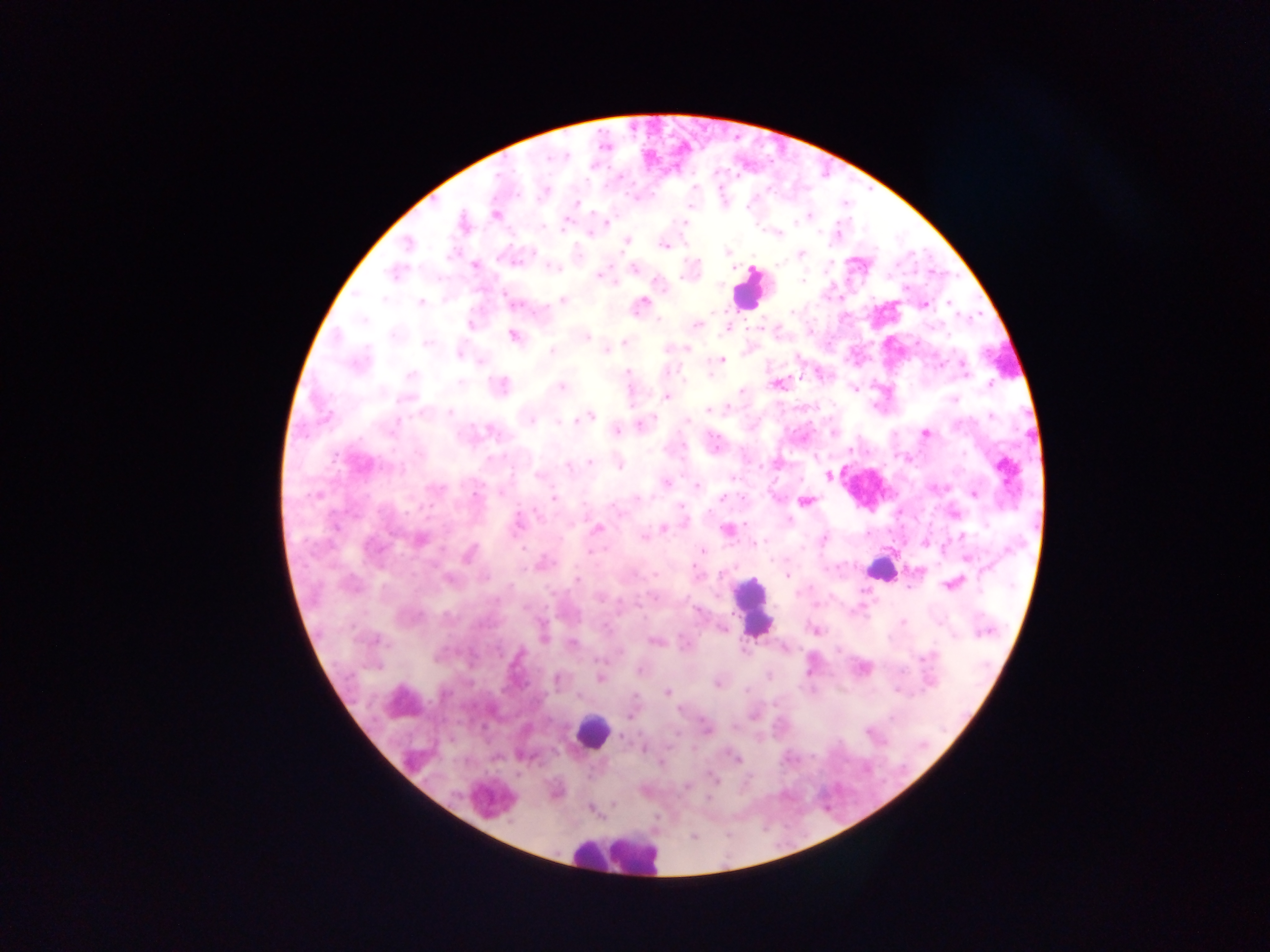

Approximate centers as {x, y} in pixels.
Summary:
  - Plasmodium parasite locations: {606, 147}, {622, 178}, {575, 202}, {496, 213}, {807, 216}, {805, 219}, {682, 223}, {544, 226}, {563, 227}, {590, 233}, {777, 235}, {626, 242}, {664, 245}, {726, 252}, {801, 254}, {852, 258}, {858, 259}, {518, 260}, {475, 265}, {631, 267}, {395, 273}, {597, 275}, {805, 279}, {356, 291}, {384, 297}, {561, 299}, {507, 301}, {641, 303}, {421, 304}, {925, 305}, {793, 313}, {363, 319}, {697, 322}, {726, 330}, {512, 335}, {585, 337}, {623, 340}, {426, 343}, {666, 348}, {605, 350}, {552, 352}, {459, 354}, {721, 358}, {479, 363}, {668, 370}, {625, 371}, {409, 375}, {777, 383}, {988, 383}, {499, 385}, {561, 387}, {740, 391}, {668, 397}, {405, 398}, {953, 400}, {715, 409}, {708, 410}, {448, 413}, {591, 417}, {397, 419}, {532, 420}, {686, 421}, {562, 425}, {640, 425}, {615, 431}, {925, 432}, {591, 463}, {567, 465}, {619, 465}, {401, 468}, {1005, 470}, {538, 474}, {828, 474}, {664, 482}, {696, 485}, {435, 489}, {935, 489}, {499, 493}, {973, 494}, {318, 496}, {552, 497}, {721, 498}, {807, 502}, {539, 518}, {516, 522}, {684, 524}, {664, 528}, {597, 530}, {726, 531}, {644, 536}, {823, 538}, {418, 542}, {754, 543}, {927, 543}, {521, 548}, {702, 552}, {593, 553}, {967, 559}, {544, 563}, {788, 577}, {446, 579}, {576, 579}, {950, 585}, {796, 591}, {654, 596}, {598, 599}, {814, 605}, {902, 621}, {723, 629}, {814, 630}, {543, 638}, {653, 641}, {572, 644}, {929, 654}, {934, 655}, {598, 661}, {638, 669}, {808, 670}, {768, 677}, {600, 678}, {558, 681}, {716, 686}, {747, 689}, {666, 693}, {898, 694}, {775, 704}, {867, 732}, {618, 737}, {624, 738}, {644, 749}, {667, 751}, {735, 759}, {662, 762}, {711, 777}, {714, 781}, {686, 787}, {707, 799}
  - Leukocyte locations: {751, 286}, {872, 571}, {751, 603}, {593, 729}, {607, 856}
  - Capture: mobile-phone photograph through a microscope
  - Field of view: single
  - Preparation: thick blood smear
  - Country: Ghana
  - Image size: 1270×952 pixels